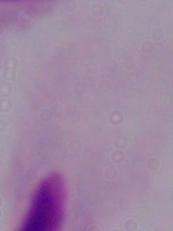
identification: trichomonad
magnification: 1000x
modality: photomicrograph